Classify this cell by malaria status.
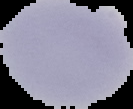
It is uninfected.

image type = cell region segmented out of the field of view; surrounding area masked to black
preparation = thin blood film
image size = 133×109 pixels